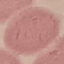

Summary:
  - Malaria status: uninfected
  - Image type: automatically extracted cell patch, resized to 64 × 64 pixels
  - Stain: Giemsa
  - Capture: smartphone through the microscope eyepiece
  - Preparation: thin blood film